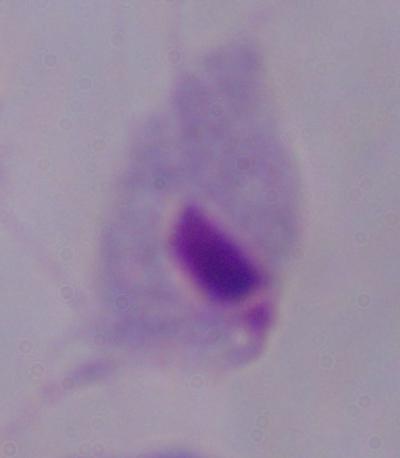
identification = trichomonad
magnification = 1000x
modality = micrograph